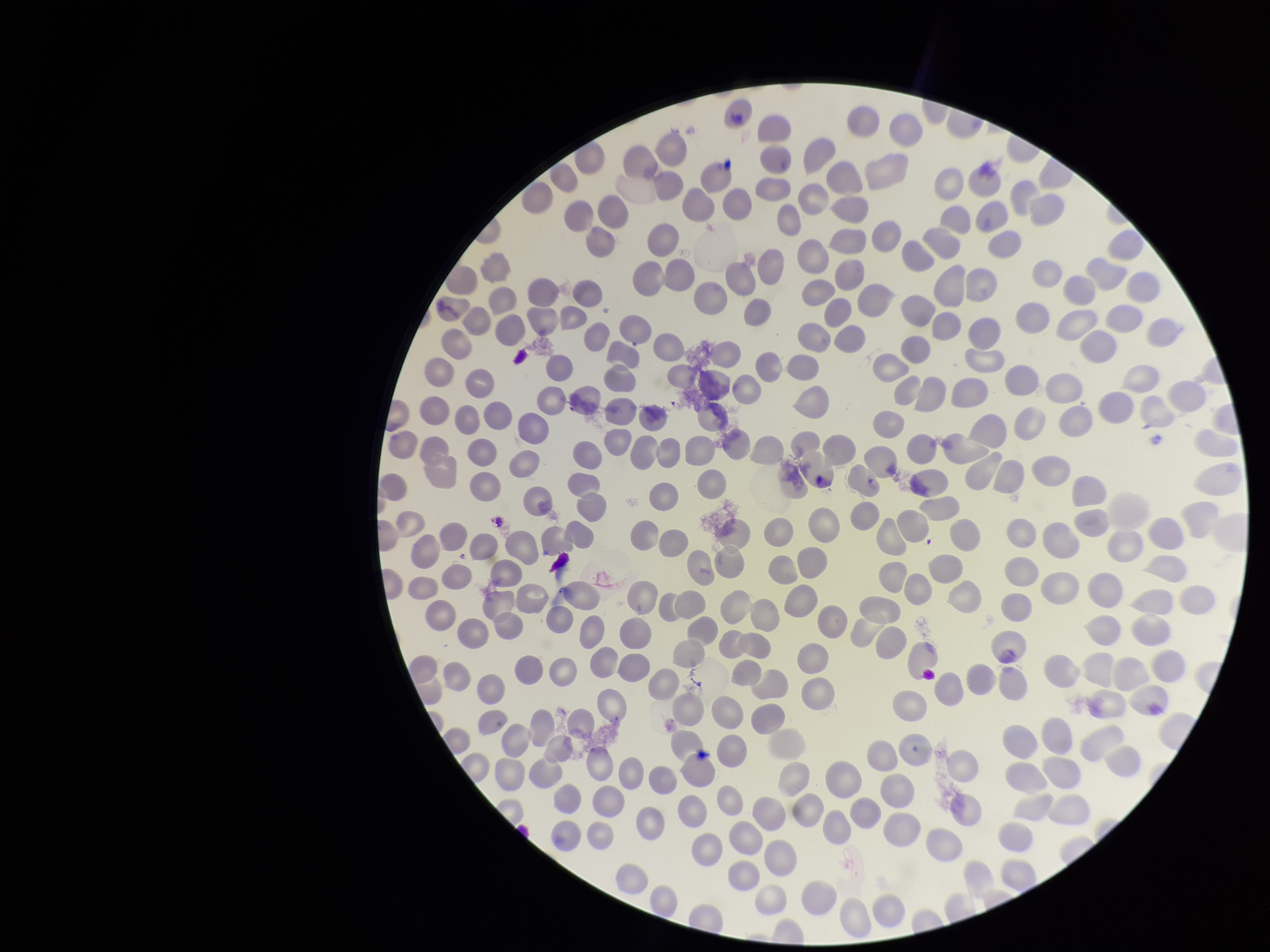

Summary:
  - Patient malaria status: negative
  - Capture: smartphone photograph through the microscope eyepiece
  - Field of view: single
  - Red blood cell count: 265
  - Parasitized red blood cells: none seen
  - Preparation: thin smear
  - Image size: 1270×952 pixels
  - Stain: Giemsa
  - Parasitized red blood cell count: 0